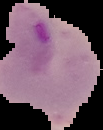
Summary:
  - Preparation: thin blood smear
  - Image size: 103×130 pixels
  - Image type: segmented cell region on a black background
  - Malaria status: parasitized